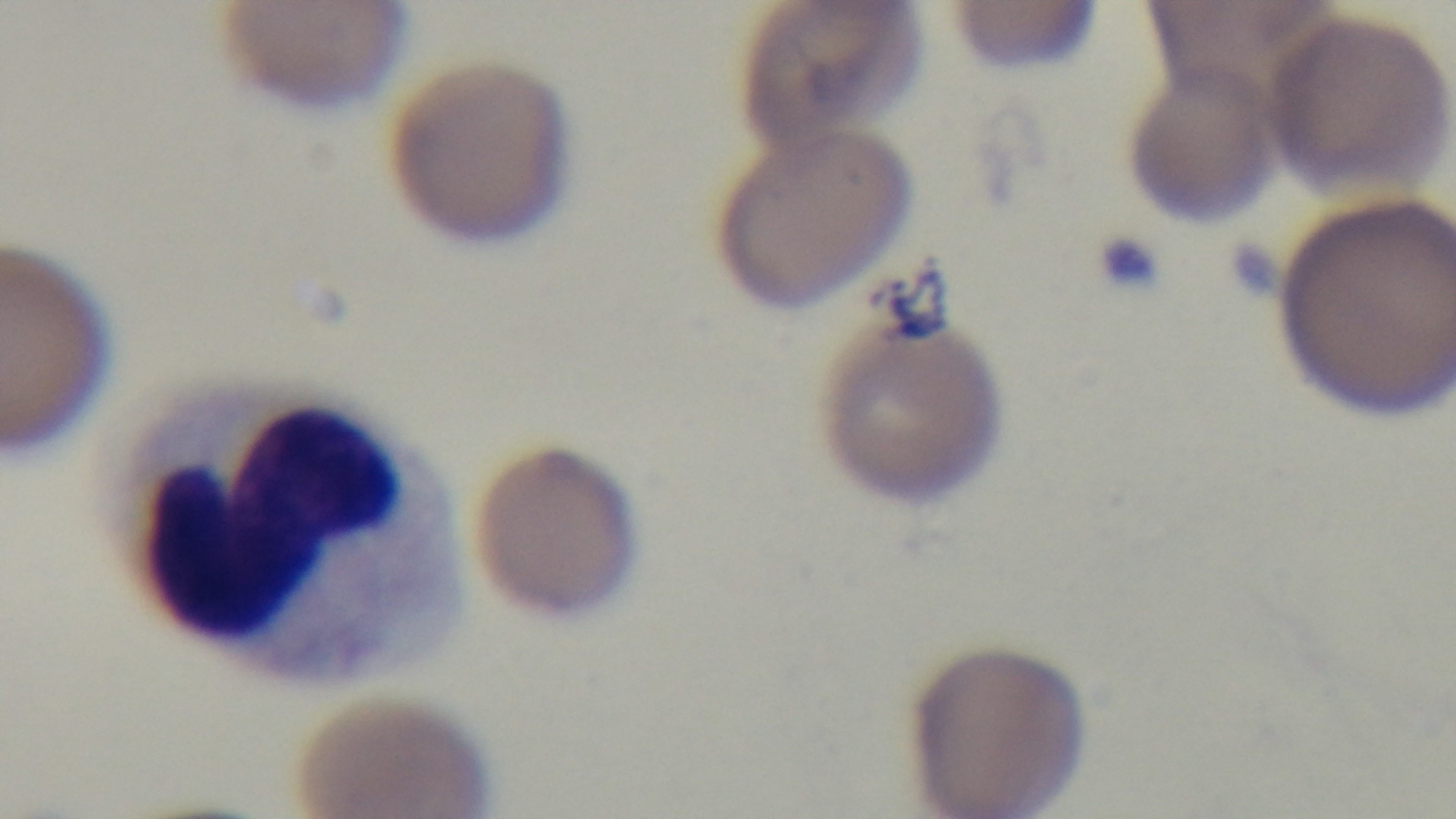 Giemsa stain. Preparation: thin smear. Malaria status: positive. Mounted 4K digital camera. Light microscopy. 100x oil-immersion objective. One field from the slide.